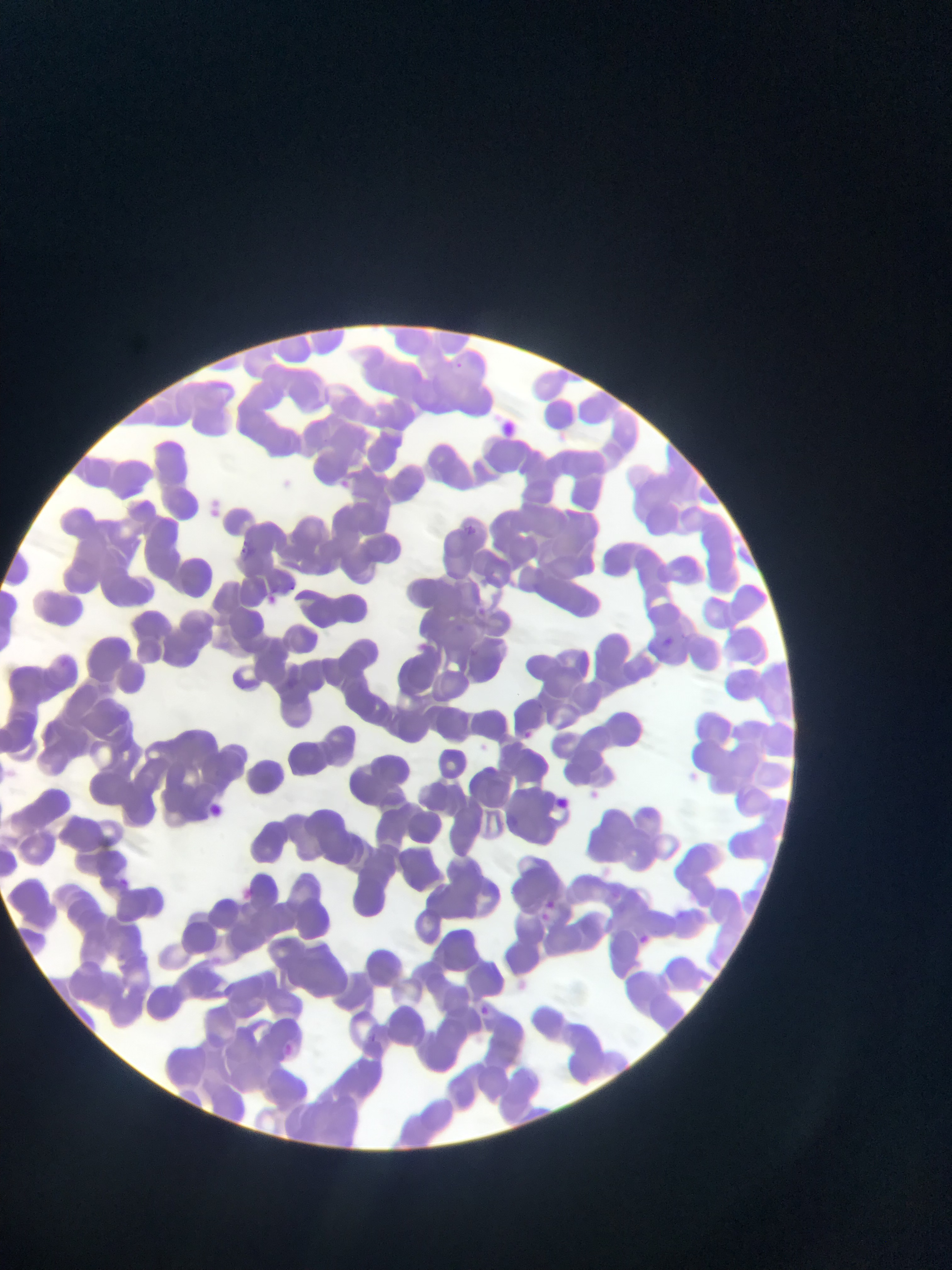
Approximate bounding boxes as [left, top, right, bottom] in pixels.
Summary:
  - Plasmodium parasite locations: [331, 474, 360, 500], [257, 588, 285, 612], [656, 632, 679, 653], [513, 725, 540, 747], [552, 793, 573, 812], [198, 799, 230, 825], [593, 861, 616, 879], [111, 873, 135, 894], [230, 884, 259, 908], [539, 896, 560, 918], [534, 902, 560, 927], [630, 928, 657, 955], [505, 975, 533, 1001], [474, 1001, 497, 1021], [356, 1029, 385, 1054], [274, 1040, 304, 1067]
  - Capture: mobile-phone photograph through a microscope
  - Image size: 952×1270 pixels
  - Preparation: thin blood film
  - Country: Ghana
  - Field of view: single